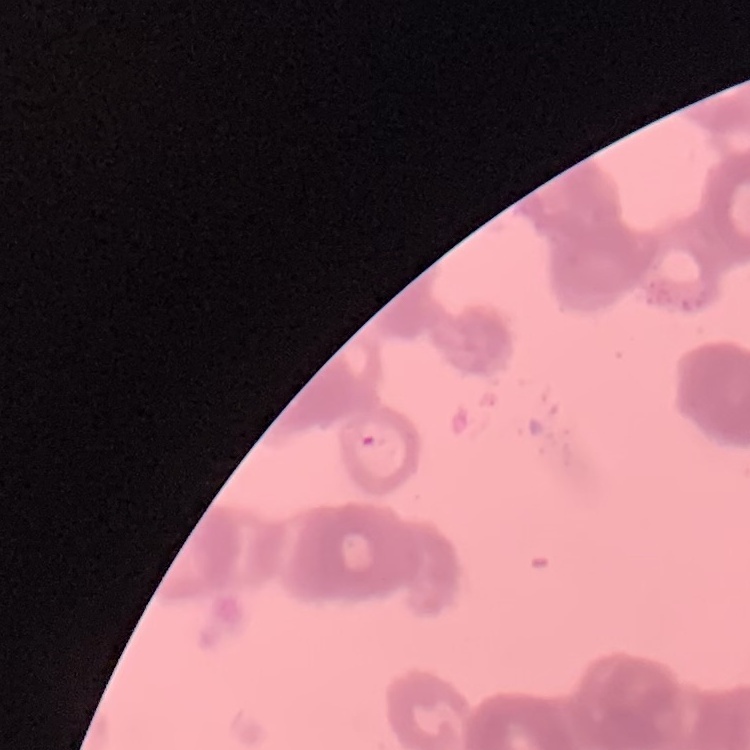

The red blood cells exhibit rouleaux formation. Thin blood smear. Stained with either Field's or Giemsa. One tile cut from a larger photomicrograph.